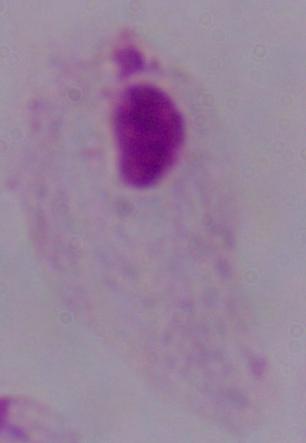
modality: micrograph
identification: trichomonad
magnification: 1000x